Classify this cell by malaria status.
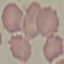
Uninfected.

Thin blood film. Giemsa stain. Photographed with a smartphone camera at the microscope eyepiece. Automatically extracted cell patch, resized to 64 × 64 pixels.